State which cell type is depicted.
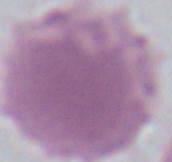
An erythrocyte.

Micrograph. 1000x magnification.